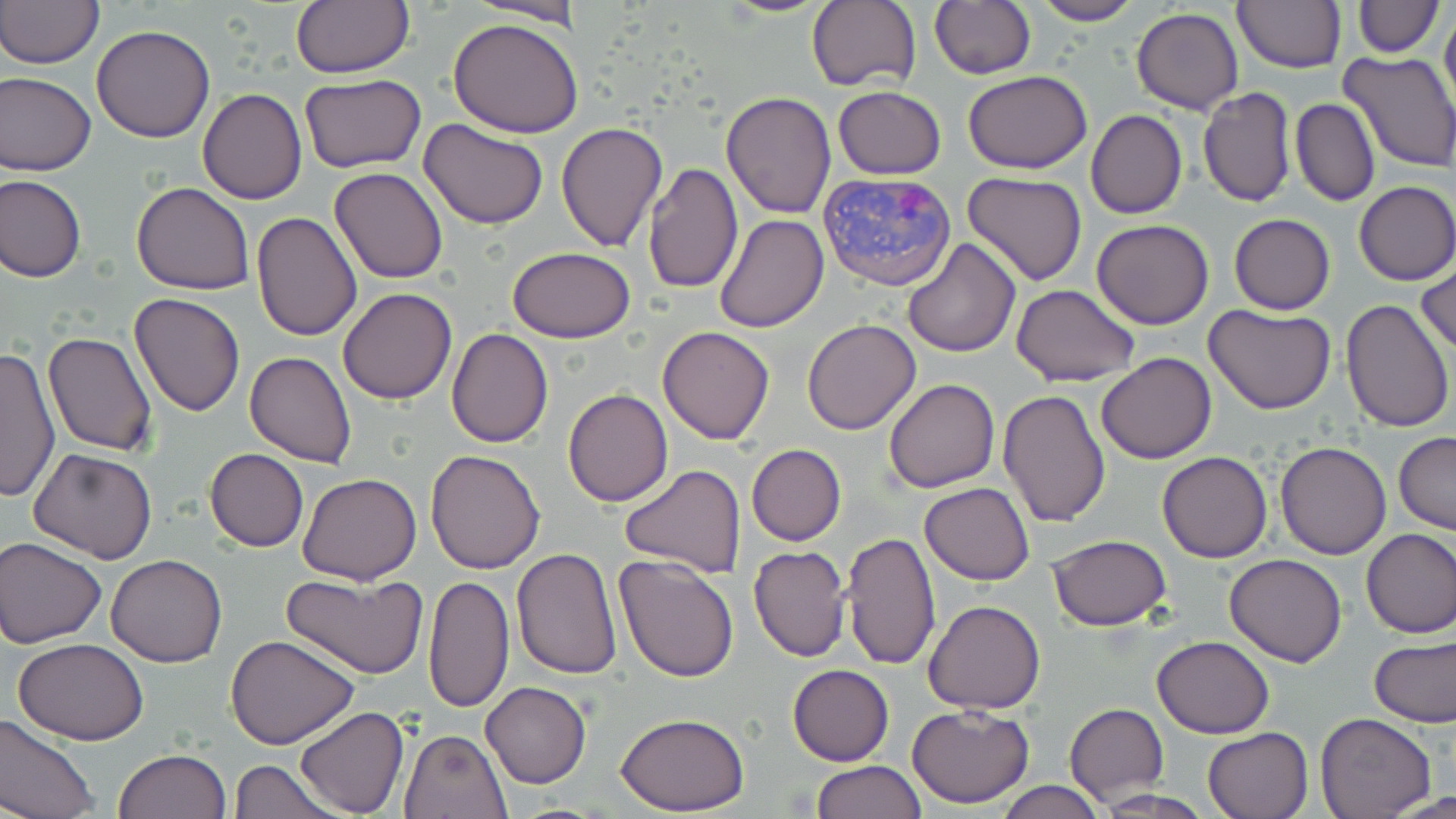 Approximate bounding boxes as (x1, y1, x2, y2) in pixels. Uninfected red blood cell locations: (0, 0, 102, 69), (291, 0, 414, 78), (710, 0, 836, 17), (1028, 0, 1145, 26), (1231, 0, 1345, 72), (807, 1, 921, 93), (930, 1, 1036, 79), (1353, 1, 1442, 56), (469, 2, 586, 25), (1130, 7, 1243, 114), (1440, 8, 1456, 115), (447, 17, 586, 137), (92, 25, 216, 144), (1339, 51, 1456, 172), (0, 70, 96, 176), (965, 71, 1092, 173), (299, 74, 427, 173), (832, 86, 947, 179), (1197, 87, 1296, 208), (197, 89, 306, 205), (719, 91, 837, 218), (1291, 99, 1380, 206), (1085, 109, 1187, 219), (419, 119, 547, 230), (556, 121, 666, 252), (642, 163, 743, 295), (330, 166, 447, 283), (963, 172, 1088, 288), (1, 174, 86, 282), (1353, 180, 1456, 284), (131, 181, 255, 296), (250, 210, 363, 341), (714, 213, 829, 332), (1228, 213, 1335, 315), (1090, 219, 1215, 330), (902, 239, 1020, 358), (508, 247, 634, 342), (1416, 260, 1455, 360), (1010, 284, 1141, 387), (337, 287, 457, 404), (129, 293, 246, 417), (1339, 297, 1454, 433), (1204, 304, 1336, 416), (803, 319, 921, 436), (656, 326, 775, 443), (446, 328, 554, 447), (43, 332, 159, 457), (0, 346, 61, 504), (245, 351, 356, 469), (1096, 352, 1217, 463), (884, 379, 999, 493), (997, 387, 1110, 528), (564, 389, 674, 506), (1393, 432, 1456, 534), (1275, 441, 1390, 560), (746, 445, 846, 546), (28, 446, 158, 565), (205, 448, 308, 550), (424, 449, 545, 574), (1158, 451, 1272, 563), (620, 465, 745, 578), (296, 473, 422, 585), (919, 482, 1036, 584), (1361, 527, 1456, 638), (841, 529, 940, 671), (1048, 535, 1173, 632), (1, 536, 106, 646), (747, 545, 851, 661), (510, 548, 624, 680), (106, 553, 227, 668), (613, 553, 741, 682), (1224, 553, 1347, 667), (281, 569, 429, 678), (423, 574, 515, 714), (924, 600, 1046, 715), (228, 634, 361, 749), (1369, 634, 1455, 729), (1152, 636, 1275, 738), (14, 639, 147, 745), (787, 664, 894, 765), (480, 680, 590, 788), (906, 703, 1034, 808), (1064, 703, 1168, 804), (295, 705, 409, 818), (1314, 712, 1437, 818), (613, 713, 750, 815), (0, 715, 100, 819), (1203, 727, 1314, 818), (398, 728, 512, 818), (116, 748, 232, 819), (231, 758, 339, 819), (813, 759, 927, 818), (996, 780, 1106, 818), (1090, 789, 1219, 818), (1382, 792, 1456, 819). Plasmodium vivax-infected red blood cell locations: (817, 170, 955, 291). Slide-level diagnosis: Plasmodium vivax. Thin blood film. May-Grünwald-Giemsa stain. Image is 1456×819 pixels. 1000x magnification. One field of a larger specimen. Optical microscopy.